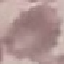

Malaria status: uninfected. Photographed with a smartphone camera at the microscope eyepiece. Automatically extracted cell patch, resized to 64 × 64 pixels. Giemsa-stained preparation. Thin smear of blood.